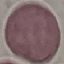
Malaria status: uninfected. Thin blood film. Cell patch, automatically extracted from a larger field of view and resized to 64 × 64 pixels. Acquired by smartphone through the microscope eyepiece. Giemsa stain.